Report the malaria status of this cell.
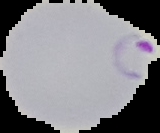
Parasitized.

Cell region segmented out of the field of view; the surrounding area is masked to black. Image is 160×133 pixels. From a thin blood smear.